Assess for malaria.
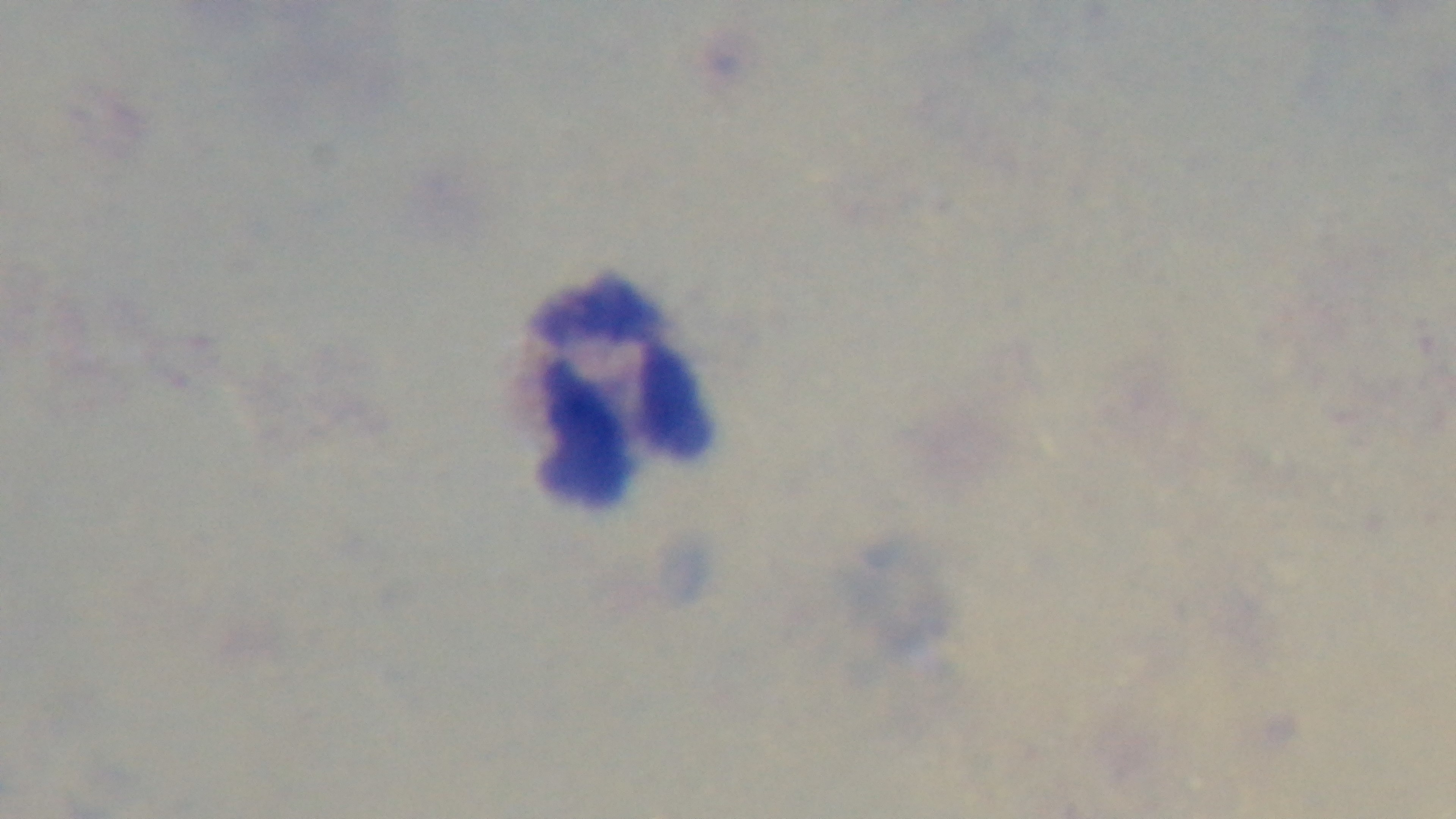
Uninfected.

Summary:
  - Preparation: thick
  - Modality: light microscopy
  - Field of view: single
  - Stain: Giemsa
  - Objective: 100x oil immersion
  - Capture: mounted 4K digital camera